Identify the parasite.
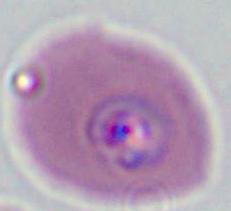

Plasmodium.

Summary:
  - Modality: micrograph
  - Magnification: 400x or 1000x